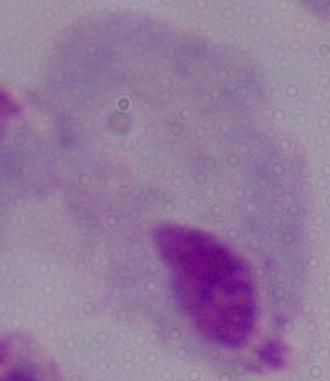 Photomicrograph. A trichomonad is seen. Captured at 1000x magnification.